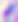

Summary:
  - Magnification: 400x
  - Identification: Toxoplasma gondii
  - Modality: micrograph